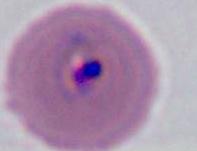

A Plasmodium parasite is seen. Micrograph. 400x or 1000x magnification.